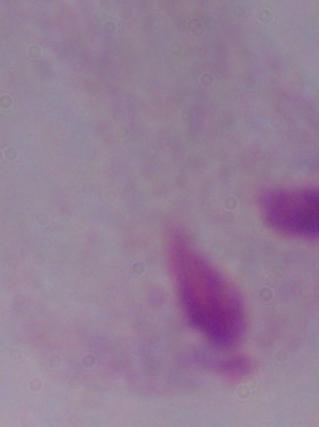
magnification = 1000x
modality = micrograph
identification = trichomonad